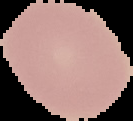

Summary:
  - Image size: 133×121 pixels
  - Image type: segmented cell region with the area outside set to black
  - Result: no Plasmodium parasites detected
  - Preparation: thin blood film